Identify the blood parasite species.
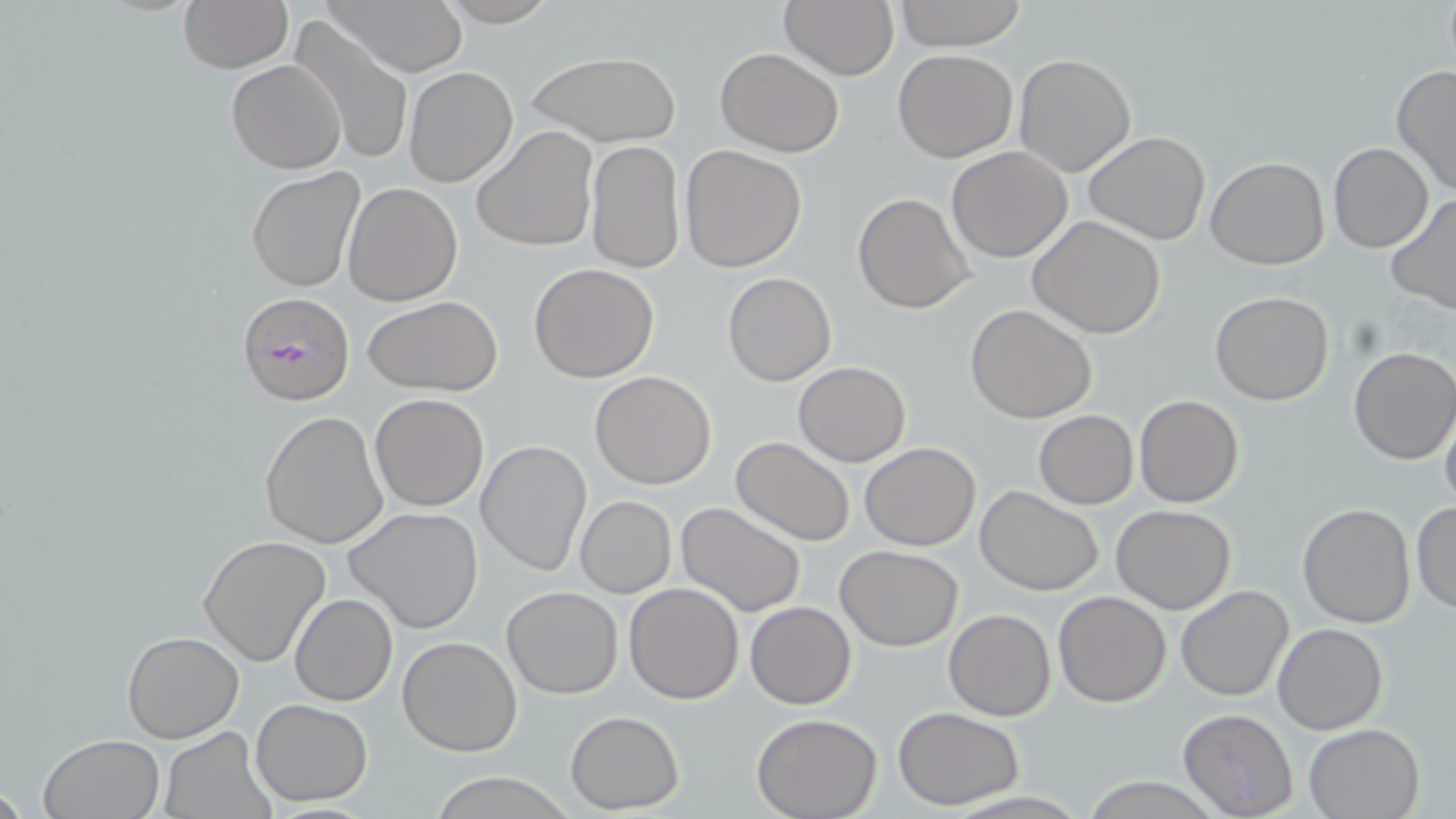

Plasmodium falciparum.

{
  "field_of_view": "one of a larger specimen",
  "plasmodium_falciparum_infected_red_blood_cell_locations": "approximate bounding boxes as (x1, y1, x2, y2) in pixels: (237, 291, 355, 407)",
  "stain": "May-Grünwald-Giemsa",
  "magnification": "1000x",
  "uninfected_red_blood_cell_locations": "approximate bounding boxes as (x1, y1, x2, y2) in pixels: (176, 0, 293, 73), (321, 0, 468, 75), (433, 0, 564, 26), (779, 0, 899, 80), (894, 0, 1027, 50), (290, 17, 413, 166), (716, 47, 844, 158), (892, 49, 1018, 162), (529, 52, 680, 147), (1012, 54, 1137, 176), (226, 59, 346, 173), (1391, 63, 1456, 198), (404, 66, 517, 185), (472, 126, 598, 253), (1084, 131, 1210, 245), (585, 141, 684, 275), (1327, 141, 1435, 252), (680, 145, 807, 272), (946, 146, 1073, 262), (1206, 157, 1330, 270), (247, 167, 365, 293), (342, 183, 462, 306), (853, 191, 975, 313), (1384, 192, 1456, 317), (1028, 216, 1168, 339), (529, 263, 660, 383), (723, 272, 836, 386), (1209, 292, 1334, 406), (363, 296, 504, 397), (965, 304, 1096, 423), (1349, 347, 1456, 464), (792, 360, 911, 466), (589, 370, 717, 490), (371, 392, 490, 511), (1134, 395, 1244, 509), (1439, 401, 1456, 518), (259, 410, 387, 549), (1034, 411, 1139, 509), (730, 437, 857, 547), (476, 438, 591, 576), (859, 442, 981, 550), (975, 485, 1103, 596), (574, 496, 676, 597), (675, 500, 807, 620), (1297, 502, 1416, 628), (1410, 502, 1456, 616), (1112, 505, 1237, 614), (344, 506, 484, 633), (197, 535, 332, 665), (835, 543, 963, 650), (624, 582, 744, 702), (1174, 585, 1293, 701), (501, 586, 623, 698), (1053, 590, 1171, 708), (290, 594, 398, 707), (746, 602, 856, 710), (943, 608, 1056, 721), (1272, 623, 1388, 735), (121, 630, 246, 743), (397, 636, 524, 757), (250, 699, 373, 804), (894, 708, 1024, 809), (1177, 709, 1299, 818), (565, 710, 684, 814), (752, 714, 882, 819), (1303, 723, 1425, 819), (159, 727, 273, 818), (39, 734, 165, 819), (433, 774, 571, 817), (1082, 776, 1223, 816)",
  "image_size": "1456×819 pixels",
  "modality": "optical microscopy",
  "preparation": "thin blood smear"
}